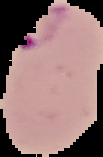

Summary:
  - Image type: segmented cell region on a black background
  - Preparation: thin blood film
  - Image size: 103×157 pixels
  - Malaria status: parasitized